Outline each blood parasite and name the species.
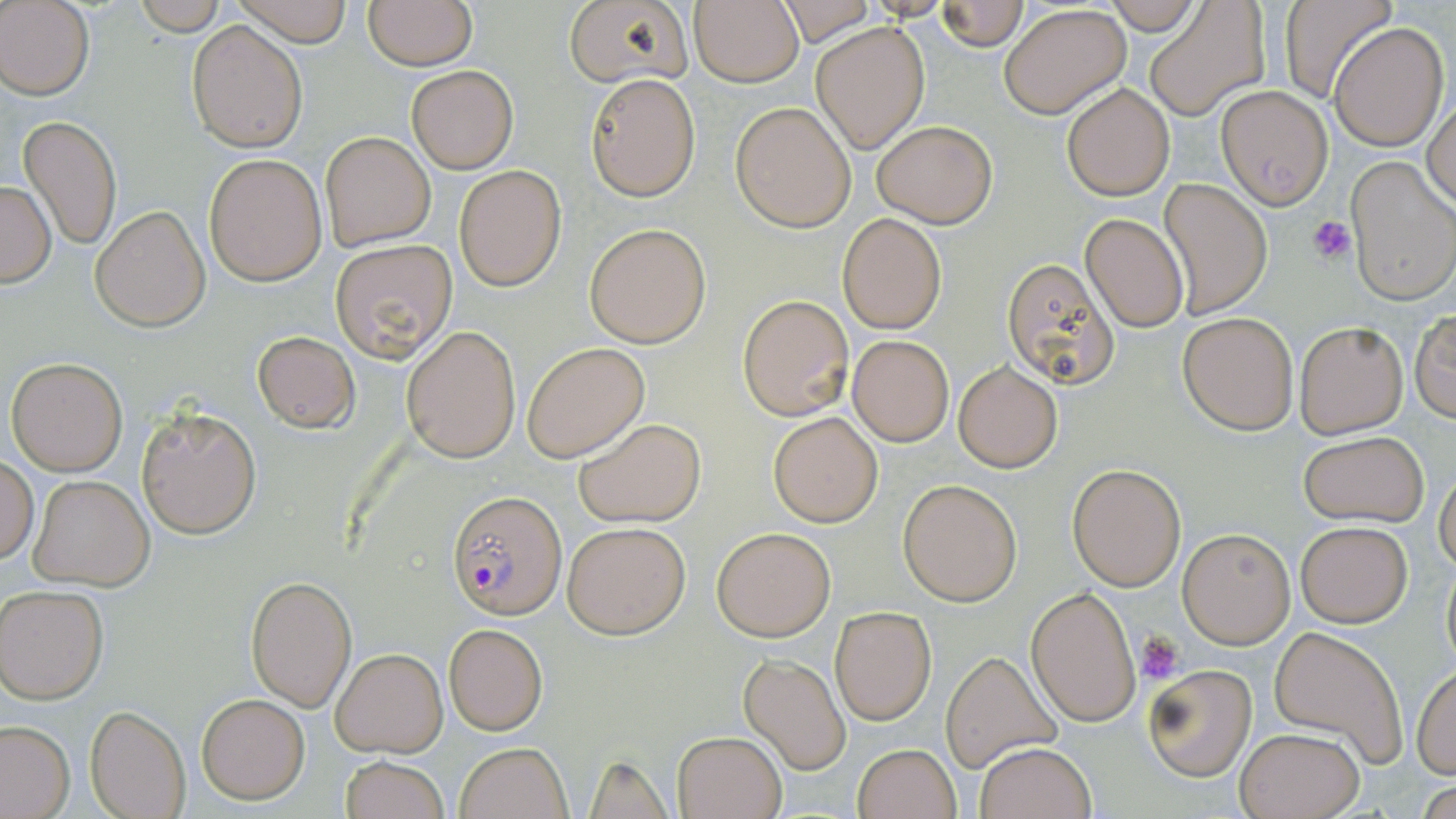
Approximate bounding boxes as named x1/y1/x2/y2 corners in pixels.
Plasmodium falciparum-infected red blood cells: (x1=447, y1=490, x2=567, y2=618).
No Plasmodium ovale, Plasmodium malariae, Plasmodium vivax, Babesia divergens, or Trypanosoma brucei observed.

slide_level_diagnosis: Plasmodium falciparum
modality: optical microscopy
preparation: thin blood smear
image_size: 1456×819 pixels
uninfected_red_blood_cell_locations: 'approximate bounding boxes as named x1/y1/x2/y2 corners in pixels: (x1=229, y1=0, x2=354, y2=46), (x1=363, y1=0, x2=477, y2=70), (x1=563, y1=0, x2=692, y2=88), (x1=1104, y1=0, x2=1202, y2=34), (x1=1279, y1=0, x2=1394, y2=103), (x1=0, y1=1, x2=94, y2=100), (x1=936, y1=1, x2=1029, y2=50), (x1=688, y1=2, x2=804, y2=86), (x1=766, y1=3, x2=879, y2=44), (x1=1000, y1=4, x2=1130, y2=117), (x1=1145, y1=5, x2=1269, y2=120), (x1=188, y1=20, x2=308, y2=153), (x1=810, y1=21, x2=929, y2=155), (x1=1329, y1=21, x2=1449, y2=151), (x1=407, y1=66, x2=518, y2=173), (x1=586, y1=73, x2=700, y2=201), (x1=1062, y1=82, x2=1174, y2=201), (x1=1215, y1=84, x2=1333, y2=208), (x1=1423, y1=95, x2=1455, y2=210), (x1=730, y1=100, x2=857, y2=233), (x1=18, y1=115, x2=123, y2=251), (x1=870, y1=119, x2=997, y2=229), (x1=320, y1=131, x2=435, y2=249), (x1=203, y1=151, x2=327, y2=286), (x1=1346, y1=155, x2=1455, y2=305), (x1=454, y1=166, x2=568, y2=291), (x1=1158, y1=179, x2=1273, y2=318), (x1=0, y1=180, x2=56, y2=287), (x1=90, y1=204, x2=212, y2=331), (x1=837, y1=212, x2=949, y2=334), (x1=1080, y1=214, x2=1190, y2=333), (x1=585, y1=223, x2=712, y2=348), (x1=330, y1=240, x2=457, y2=364), (x1=1000, y1=256, x2=1118, y2=391), (x1=737, y1=294, x2=853, y2=421), (x1=1411, y1=309, x2=1455, y2=421), (x1=1176, y1=312, x2=1300, y2=434), (x1=1295, y1=320, x2=1410, y2=439), (x1=403, y1=325, x2=521, y2=464), (x1=252, y1=329, x2=360, y2=433), (x1=847, y1=335, x2=953, y2=447), (x1=522, y1=342, x2=650, y2=463), (x1=6, y1=354, x2=129, y2=476), (x1=953, y1=361, x2=1062, y2=473), (x1=138, y1=403, x2=261, y2=539), (x1=768, y1=411, x2=884, y2=527), (x1=574, y1=418, x2=705, y2=527), (x1=1297, y1=432, x2=1429, y2=526), (x1=0, y1=455, x2=39, y2=566), (x1=1066, y1=462, x2=1186, y2=592), (x1=1434, y1=469, x2=1456, y2=578), (x1=28, y1=474, x2=154, y2=591), (x1=897, y1=479, x2=1022, y2=606), (x1=1295, y1=520, x2=1412, y2=628), (x1=562, y1=521, x2=690, y2=639), (x1=712, y1=526, x2=835, y2=641), (x1=1176, y1=527, x2=1297, y2=649), (x1=1440, y1=549, x2=1455, y2=676), (x1=244, y1=575, x2=355, y2=709), (x1=0, y1=583, x2=109, y2=704), (x1=1026, y1=585, x2=1141, y2=729), (x1=830, y1=607, x2=936, y2=725), (x1=443, y1=623, x2=547, y2=735), (x1=1269, y1=625, x2=1409, y2=764), (x1=331, y1=647, x2=448, y2=756), (x1=940, y1=652, x2=1059, y2=772), (x1=737, y1=653, x2=851, y2=773), (x1=1142, y1=664, x2=1258, y2=783), (x1=1412, y1=664, x2=1455, y2=779), (x1=196, y1=693, x2=311, y2=805), (x1=85, y1=704, x2=191, y2=819), (x1=0, y1=721, x2=75, y2=818), (x1=1234, y1=727, x2=1365, y2=819), (x1=673, y1=730, x2=787, y2=819), (x1=454, y1=742, x2=574, y2=819), (x1=974, y1=742, x2=1096, y2=819), (x1=853, y1=743, x2=959, y2=819), (x1=582, y1=753, x2=676, y2=818), (x1=340, y1=754, x2=448, y2=819)'
platelet_locations: 'approximate bounding boxes as named x1/y1/x2/y2 corners in pixels: (x1=1310, y1=215, x2=1355, y2=265), (x1=1137, y1=632, x2=1185, y2=683)'
magnification: 1000x
field_of_view: single
stain: May-Grünwald-Giemsa